State which parasite is depicted.
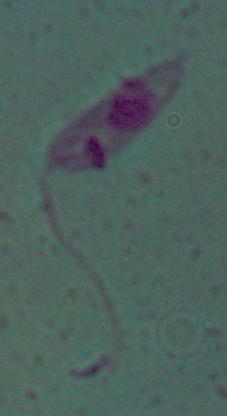

Leishmania.

1000x magnification. Micrograph.